Describe the morphology of the red blood cells.
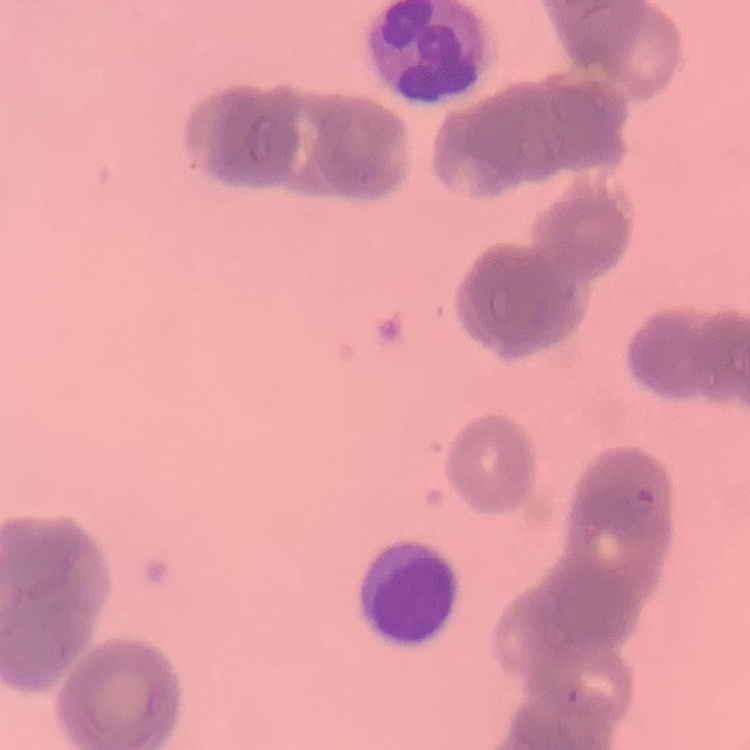

Rouleaux formation.

stain: Field's or Giemsa
preparation: thin blood smear
image_type: one tile cut from a larger photomicrograph